State the blood parasite species.
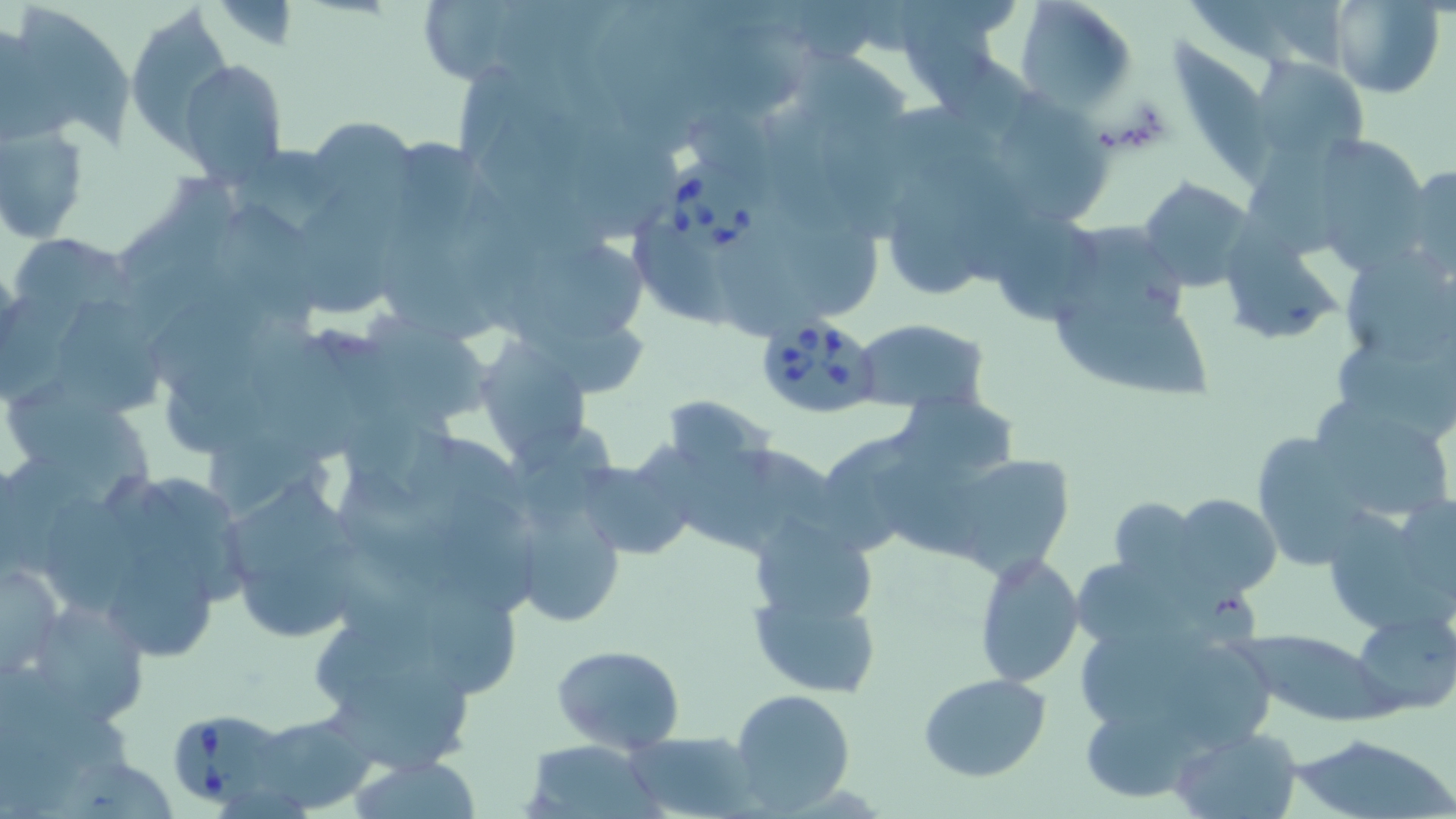
Babesia divergens.

Summary:
  - Coordinate format: approximate bounding boxes as (x1,y1)-(x2,y2) corner pairs in pixels
  - Babesia divergens-infected red blood cell locations: (658,154)-(763,256), (753,314)-(883,418), (166,706)-(289,809)
  - Uninfected red blood cell locations: (892,0)-(1020,100), (1015,0)-(1137,112), (1322,0)-(1441,96), (3,4)-(135,147), (128,6)-(233,144), (1174,39)-(1281,184), (794,52)-(913,136), (1247,54)-(1371,170), (178,58)-(287,183), (997,92)-(1111,220), (305,114)-(418,216), (1,120)-(87,243), (575,124)-(680,241), (1324,135)-(1438,275), (1249,152)-(1361,259), (1400,163)-(1456,283), (1138,177)-(1255,291), (891,188)-(984,293), (303,198)-(400,307), (216,205)-(326,329), (997,208)-(1110,325), (789,221)-(880,316), (639,223)-(731,329), (1223,226)-(1337,343), (535,241)-(653,344), (1346,251)-(1455,358), (1056,293)-(1219,400), (61,299)-(162,413), (364,314)-(495,417), (852,319)-(988,412), (252,336)-(356,463), (472,336)-(595,464), (1335,340)-(1456,439), (163,359)-(280,456), (11,391)-(161,489), (1306,392)-(1453,522), (895,394)-(1026,465), (1259,435)-(1368,568), (575,451)-(697,560), (875,453)-(977,555), (942,453)-(1074,575), (342,467)-(451,597), (233,470)-(352,583), (435,488)-(534,614), (1170,493)-(1280,599), (49,496)-(138,613), (1105,496)-(1204,588), (511,498)-(627,630), (1334,507)-(1456,629), (747,517)-(885,701), (244,545)-(365,636), (109,550)-(223,664), (975,550)-(1084,686), (0,561)-(64,676), (1077,561)-(1201,639), (418,589)-(517,699), (21,594)-(153,731), (1354,611)-(1456,715), (1237,625)-(1392,726), (1083,628)-(1230,721), (1183,640)-(1276,751), (551,644)-(686,753), (327,665)-(478,775), (920,674)-(1052,782), (729,688)-(854,812), (1081,696)-(1206,803), (247,711)-(376,813), (1165,725)-(1302,817), (622,728)-(757,816), (1289,732)-(1453,819), (522,740)-(662,818), (350,753)-(484,819)
  - Modality: light microscopy
  - Stain: May-Grünwald-Giemsa
  - Field of view: single
  - Magnification: 1000x
  - Preparation: thin blood smear
  - Image size: 1456×819 pixels